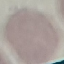

Malaria status: uninfected. Automatically extracted cell patch, resized to 64 × 64 pixels. Giemsa stain. Thin blood smear. Photographed with a smartphone camera at the microscope eyepiece.